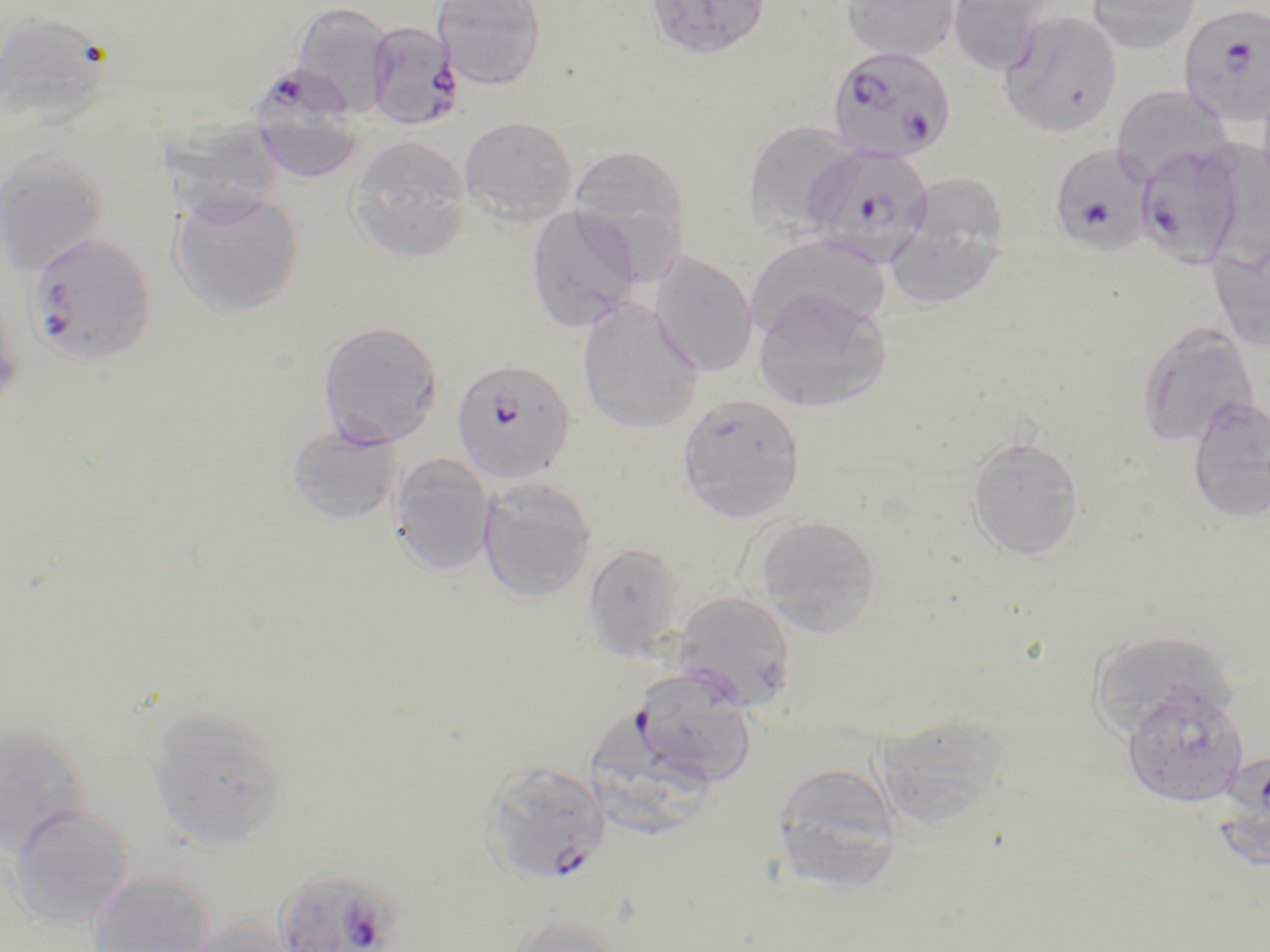

slide-level diagnosis = Plasmodium falciparum
preparation = thin blood smear
field of view = single
Plasmodium falciparum-infected red blood cell locations = approximate bounding boxes as (x1, y1, x2, y2) in pixels: (1178, 3, 1270, 127), (365, 20, 462, 130), (827, 45, 957, 163), (254, 67, 361, 183), (1048, 143, 1156, 256), (1133, 143, 1250, 269), (803, 145, 934, 267), (28, 231, 156, 366), (451, 358, 576, 484), (630, 670, 757, 790), (481, 760, 611, 884), (276, 865, 407, 952)
image size = 1270×952 pixels
stain = May-Grünwald-Giemsa
modality = light microscopy
uninfected red blood cell locations = approximate bounding boxes as (x1, y1, x2, y2) in pixels: (433, 0, 548, 90), (648, 0, 775, 59), (841, 0, 961, 63), (946, 0, 1054, 76), (1086, 0, 1201, 55), (288, 1, 397, 119), (0, 10, 118, 129), (998, 10, 1123, 138), (1256, 77, 1270, 200), (1111, 85, 1233, 183), (160, 110, 286, 226), (460, 115, 578, 225), (742, 120, 862, 235), (348, 135, 472, 263), (568, 145, 692, 283), (0, 149, 108, 277), (171, 189, 304, 317), (882, 191, 1010, 311), (526, 205, 642, 333), (746, 234, 892, 341), (1208, 239, 1270, 352), (649, 251, 758, 376), (752, 289, 894, 414), (0, 292, 24, 420), (578, 299, 703, 434), (318, 320, 443, 448), (1134, 321, 1259, 447), (676, 393, 806, 523), (1185, 396, 1270, 524), (285, 422, 402, 525), (967, 435, 1085, 561), (390, 454, 495, 575), (478, 476, 597, 603), (753, 515, 883, 637), (583, 542, 685, 660), (673, 591, 798, 712), (1085, 630, 1241, 742), (1121, 685, 1249, 809), (885, 709, 1009, 836), (147, 710, 286, 849), (590, 716, 715, 840), (0, 723, 91, 856), (771, 761, 902, 889), (7, 804, 135, 930), (87, 871, 214, 952), (503, 914, 629, 952), (185, 918, 300, 952)
magnification = 1000x